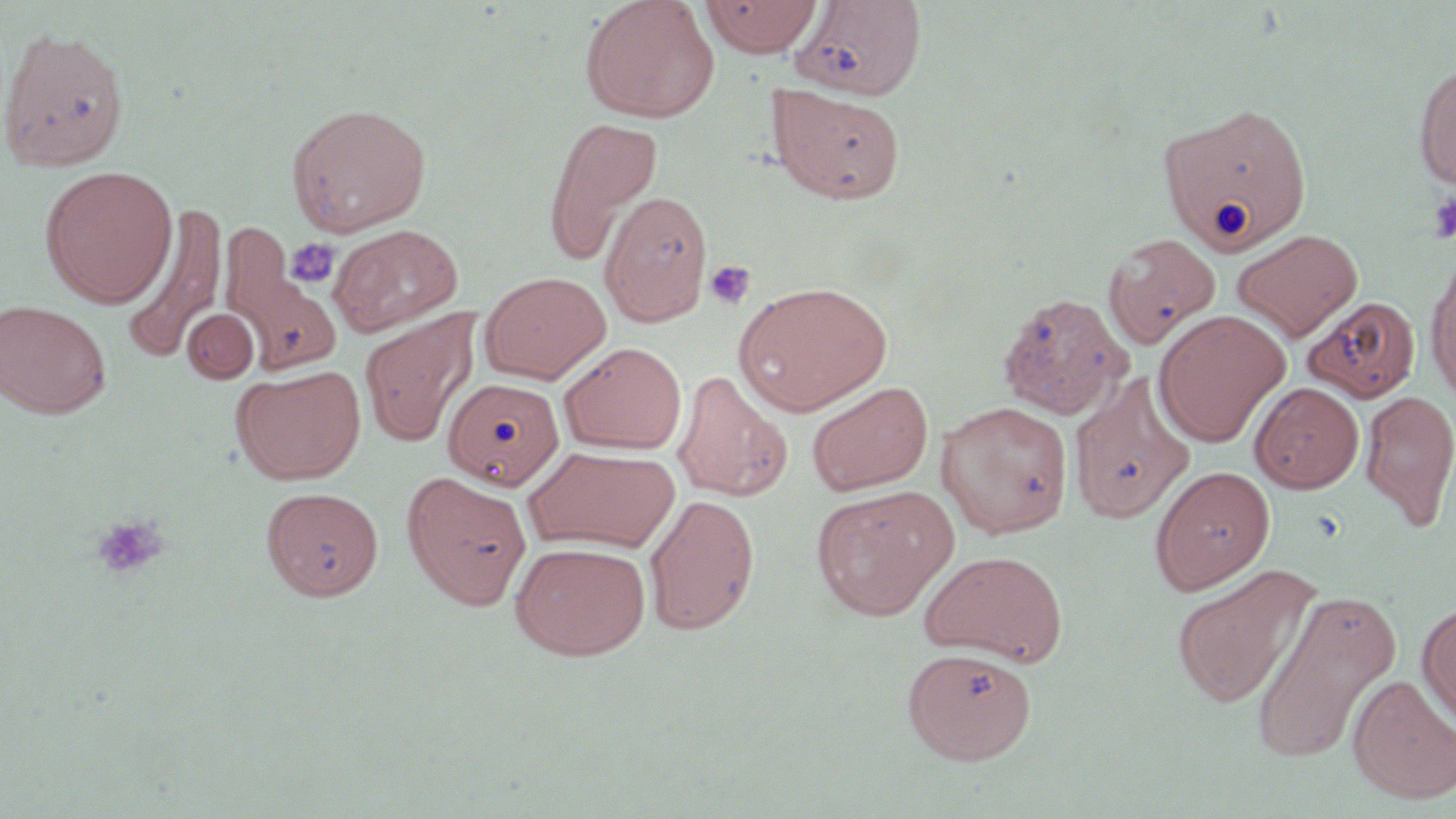

slide-level diagnosis = negative for blood parasites
image size = 1456×819 pixels
modality = light microscopy
magnification = 1000x
platelet locations = approximate bounding boxes as (x1,y1)-(x2,y2) corner pairs in pixels: (1426,191)-(1456,243), (284,238)-(339,287), (705,260)-(756,310), (91,514)-(168,580)
preparation = thin blood film
stain = May-Grünwald-Giemsa
field of view = single
uninfected red blood cell locations = approximate bounding boxes as (x1,y1)-(x2,y2) corner pairs in pixels: (580,0)-(720,123), (699,0)-(825,56), (790,1)-(927,100), (0,26)-(130,172), (1413,63)-(1456,190), (768,85)-(905,204), (286,101)-(432,236), (1158,101)-(1313,257), (541,115)-(664,266), (39,165)-(178,308), (599,189)-(713,327), (121,205)-(228,361), (329,223)-(463,337), (1232,229)-(1362,341), (1103,232)-(1221,348), (223,240)-(342,378), (1425,253)-(1456,405), (479,271)-(611,384), (734,280)-(892,416), (997,292)-(1131,420), (1302,294)-(1421,403), (0,299)-(112,419), (181,308)-(259,383), (1153,308)-(1290,446), (360,311)-(477,447), (560,342)-(687,454), (232,364)-(366,486), (672,370)-(792,503), (444,377)-(564,490), (807,381)-(933,496), (1068,381)-(1194,524), (1250,382)-(1364,493), (1359,389)-(1456,530), (936,401)-(1073,537), (524,446)-(679,555), (1150,465)-(1275,594), (401,471)-(533,611), (810,485)-(959,621), (262,486)-(384,601), (644,494)-(760,636), (509,541)-(651,661), (919,550)-(1069,667), (1170,563)-(1319,709), (1250,589)-(1401,765), (1417,601)-(1456,725), (902,646)-(1037,764), (1348,674)-(1456,804)